Name the parasite shown.
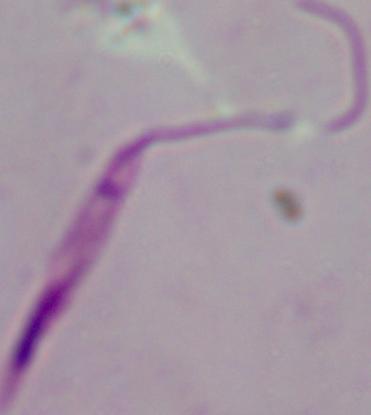
Leishmania.

1000x magnification. Photomicrograph.